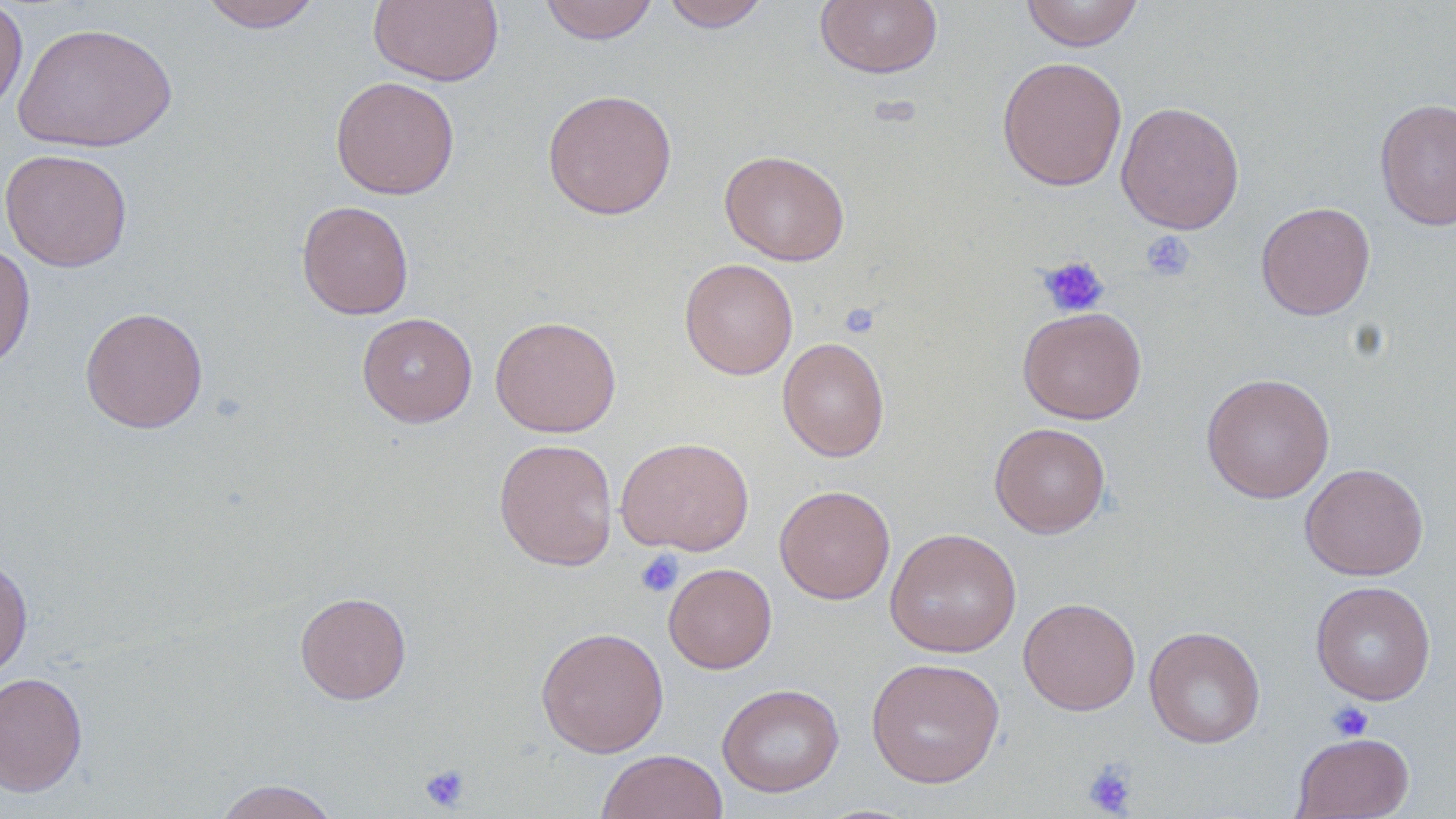
Summary:
  - Coordinate format: approximate bounding boxes as [x1, y1, x2, y2] in pixels
  - Uninfected red blood cell locations: [196, 0, 323, 32], [368, 0, 504, 87], [539, 0, 658, 44], [660, 0, 773, 32], [1020, 0, 1145, 52], [0, 1, 29, 119], [814, 1, 943, 79], [13, 21, 178, 153], [996, 56, 1127, 191], [330, 76, 460, 199], [542, 88, 678, 220], [1375, 97, 1456, 231], [1115, 100, 1245, 235], [0, 148, 133, 272], [719, 150, 850, 265], [296, 200, 414, 320], [1256, 201, 1375, 320], [0, 240, 36, 371], [679, 258, 798, 380], [80, 306, 208, 434], [1017, 306, 1147, 424], [357, 312, 478, 427], [490, 315, 622, 437], [777, 337, 889, 462], [1200, 372, 1335, 503], [989, 422, 1110, 538], [616, 436, 755, 555], [494, 438, 618, 571], [1300, 462, 1429, 580], [774, 484, 895, 604], [884, 527, 1021, 658], [0, 557, 33, 681], [663, 562, 777, 674], [1310, 580, 1436, 705], [295, 591, 412, 704], [1018, 596, 1141, 715], [1144, 625, 1266, 749], [535, 626, 669, 758], [866, 657, 1005, 788], [0, 671, 88, 797], [717, 683, 845, 798], [1291, 731, 1415, 818], [596, 750, 728, 819], [213, 779, 342, 819]
  - Platelet locations: [1139, 230, 1196, 282], [1038, 255, 1110, 318], [635, 550, 684, 598], [1327, 701, 1373, 741], [1082, 759, 1139, 817], [419, 763, 470, 812]
  - Slide-level diagnosis: negative for blood parasites
  - Magnification: 1000x
  - Modality: light microscopy
  - Stain: May-Grünwald-Giemsa
  - Preparation: thin blood film
  - Field of view: one of a larger specimen
  - Image size: 1456×819 pixels